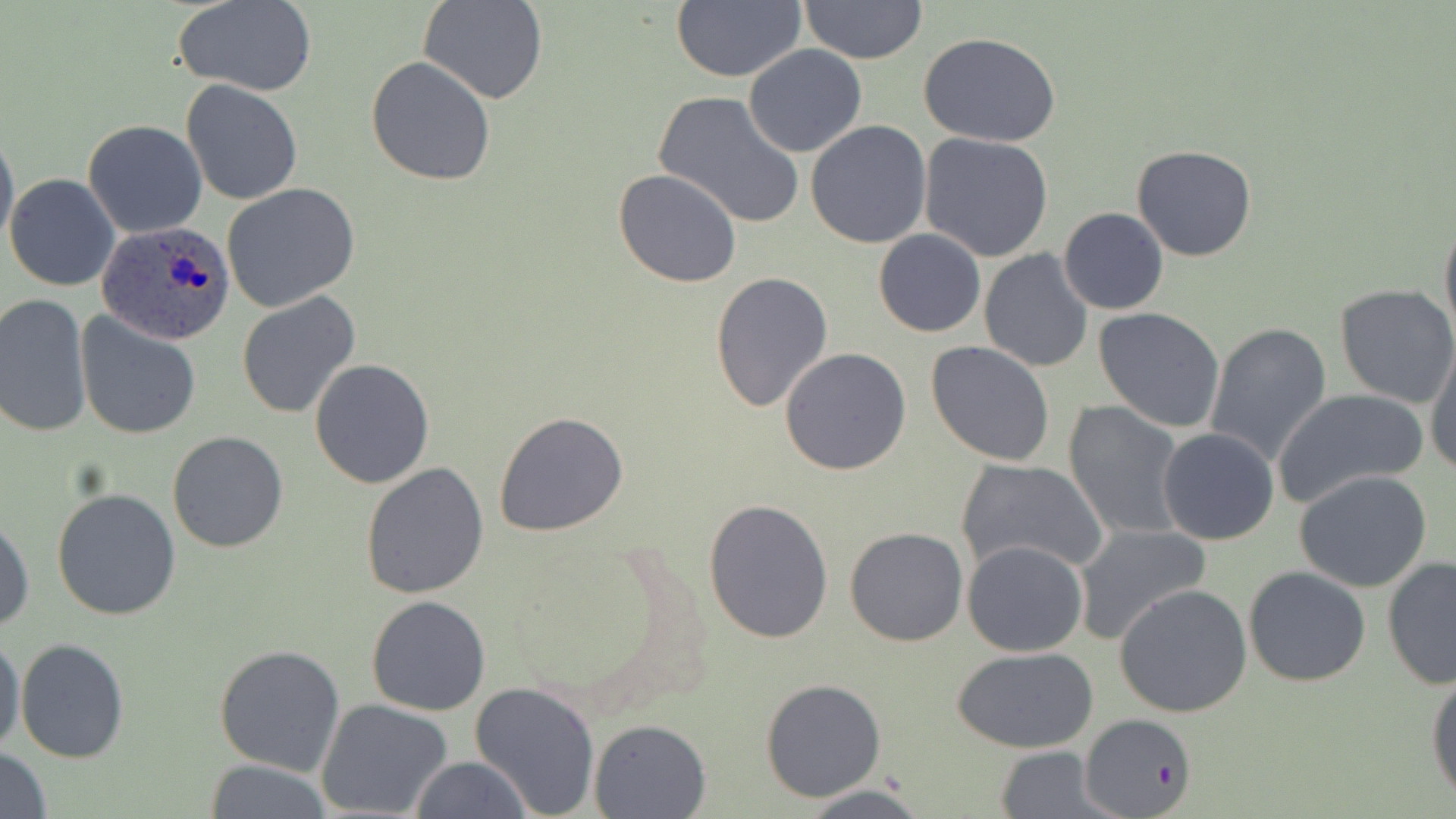
Summary:
  - Coordinate format: approximate bounding boxes as (x1, y1, x2, y2) in pixels
  - Uninfected red blood cell locations: (420, 0, 546, 105), (671, 0, 806, 83), (799, 0, 928, 65), (172, 1, 318, 97), (918, 32, 1063, 148), (743, 44, 867, 159), (366, 56, 496, 187), (181, 81, 303, 205), (651, 89, 806, 229), (83, 119, 208, 238), (805, 119, 932, 250), (0, 125, 18, 254), (918, 132, 1056, 262), (1132, 145, 1257, 262), (613, 168, 741, 288), (5, 174, 120, 292), (220, 182, 361, 312), (1058, 208, 1169, 315), (1439, 215, 1456, 347), (873, 229, 986, 338), (978, 248, 1094, 373), (710, 271, 833, 412), (1334, 283, 1456, 409), (237, 291, 362, 421), (0, 293, 93, 439), (1094, 307, 1225, 432), (76, 310, 201, 442), (1204, 323, 1333, 470), (1424, 336, 1456, 478), (925, 341, 1057, 467), (779, 348, 912, 476), (309, 358, 435, 488), (1272, 390, 1427, 507), (1064, 401, 1186, 540), (495, 411, 628, 537), (1157, 428, 1281, 546), (166, 430, 289, 552), (954, 459, 1108, 578), (360, 461, 491, 599), (1295, 470, 1433, 592), (52, 486, 183, 620), (702, 497, 836, 644), (0, 513, 34, 633), (1073, 523, 1212, 647), (843, 527, 967, 647), (962, 539, 1090, 657), (1382, 557, 1456, 689), (1242, 565, 1371, 687), (1115, 584, 1254, 719), (367, 595, 491, 715), (0, 628, 25, 759), (15, 637, 130, 764), (214, 645, 345, 776), (952, 645, 1101, 753), (1427, 667, 1456, 805), (760, 678, 886, 802), (470, 679, 600, 818), (316, 698, 454, 818), (1081, 714, 1197, 819), (588, 719, 710, 818), (0, 745, 51, 818), (992, 746, 1115, 818), (410, 756, 532, 819), (203, 759, 337, 818), (799, 785, 930, 817)
  - Plasmodium ovale-infected red blood cell locations: (97, 220, 235, 346)
  - Slide-level diagnosis: Plasmodium ovale
  - Modality: light microscopy
  - Preparation: thin blood smear
  - Stain: May-Grünwald-Giemsa
  - Magnification: 1000x
  - Image size: 1456×819 pixels
  - Field of view: one of a larger specimen